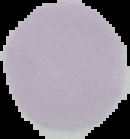
Summary:
  - Malaria status: uninfected
  - Preparation: thin blood smear
  - Image type: segmented cell region with the area outside set to black
  - Image size: 130×139 pixels